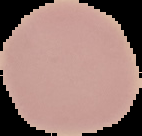
Summary:
  - Preparation: thin blood smear
  - Image size: 142×136 pixels
  - Result: negative for Plasmodium parasites
  - Image type: segmented cell region on a black background